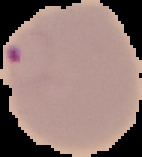

preparation = thin blood smear
result = malaria parasites identified
image size = 142×157 pixels
image type = cell region segmented out of the field of view; surrounding area masked to black